State the preparation type.
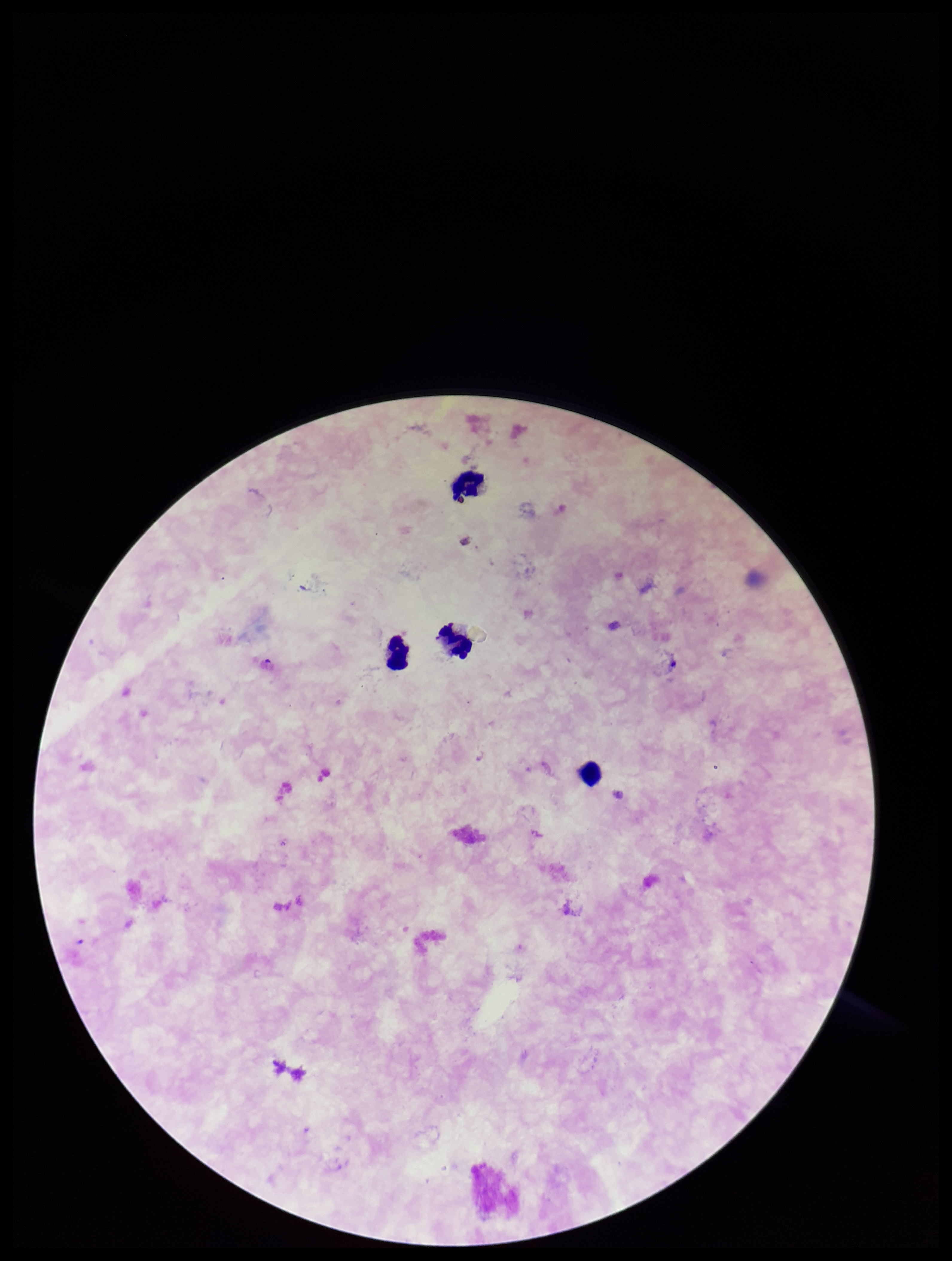

Thick.

Summary:
  - Leukocyte count: 4
  - Capture: smartphone photograph through the microscope eyepiece
  - Field of view: one from this slide
  - Stain: Giemsa
  - Parasite count: 0
  - Plasmodium parasites: none identified
  - Patient malaria status: negative
  - Image size: 952×1261 pixels